Give the position of every malaria parasite.
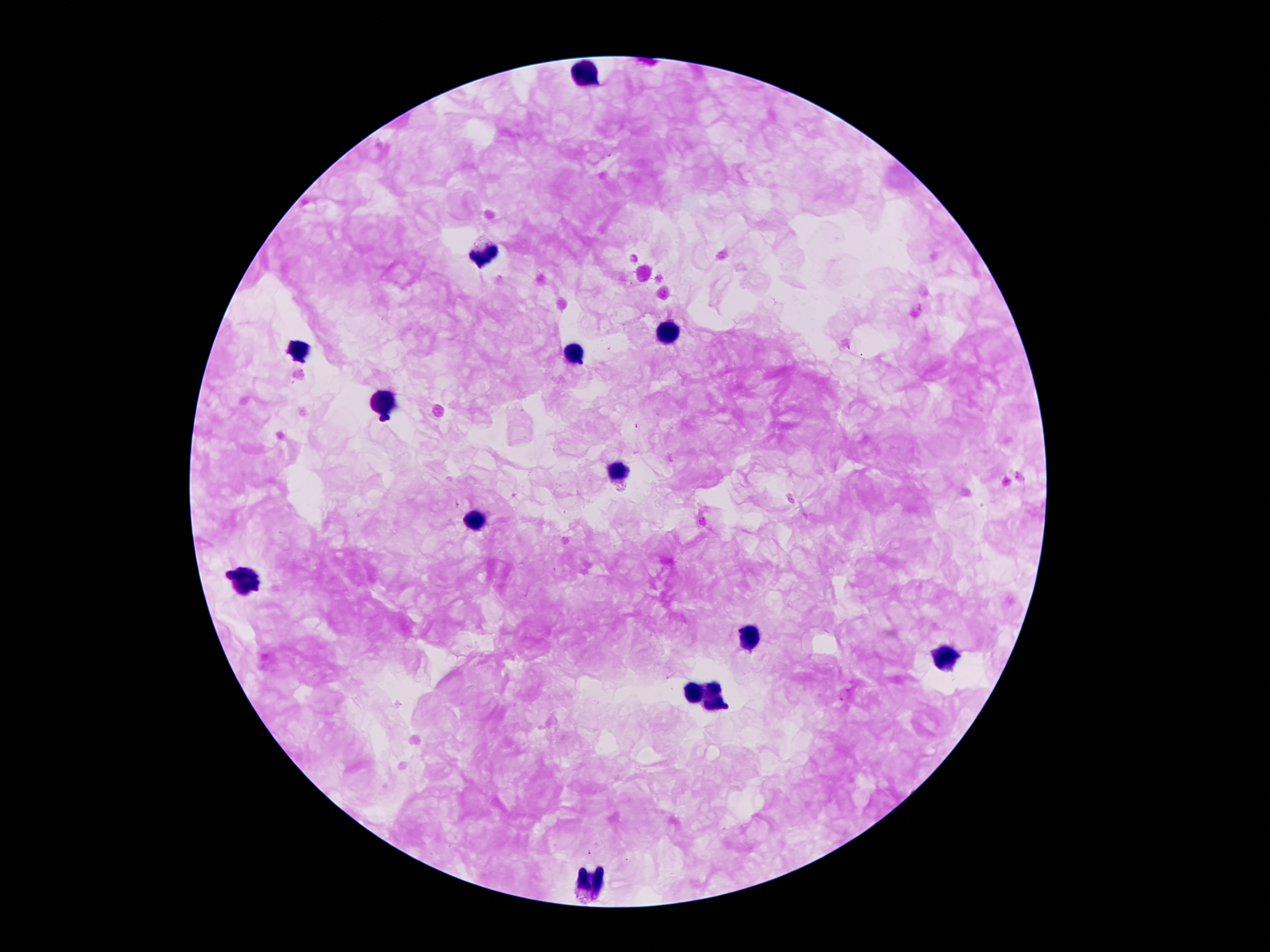
Approximate centers as {x, y} in pixels.
Malaria parasites: {588, 853}.

leukocyte locations = {585, 70}, {485, 258}, {667, 330}, {577, 353}, {297, 355}, {384, 406}, {619, 470}, {473, 521}, {246, 579}, {746, 638}, {944, 661}, {694, 693}, {713, 698}, {590, 884}
stain = Giemsa
preparation = thick blood film
field of view = single
patient malaria status = positive for Plasmodium falciparum
image size = 1270×952 pixels
capture = smartphone camera through the microscope eyepiece
magnification = 100x